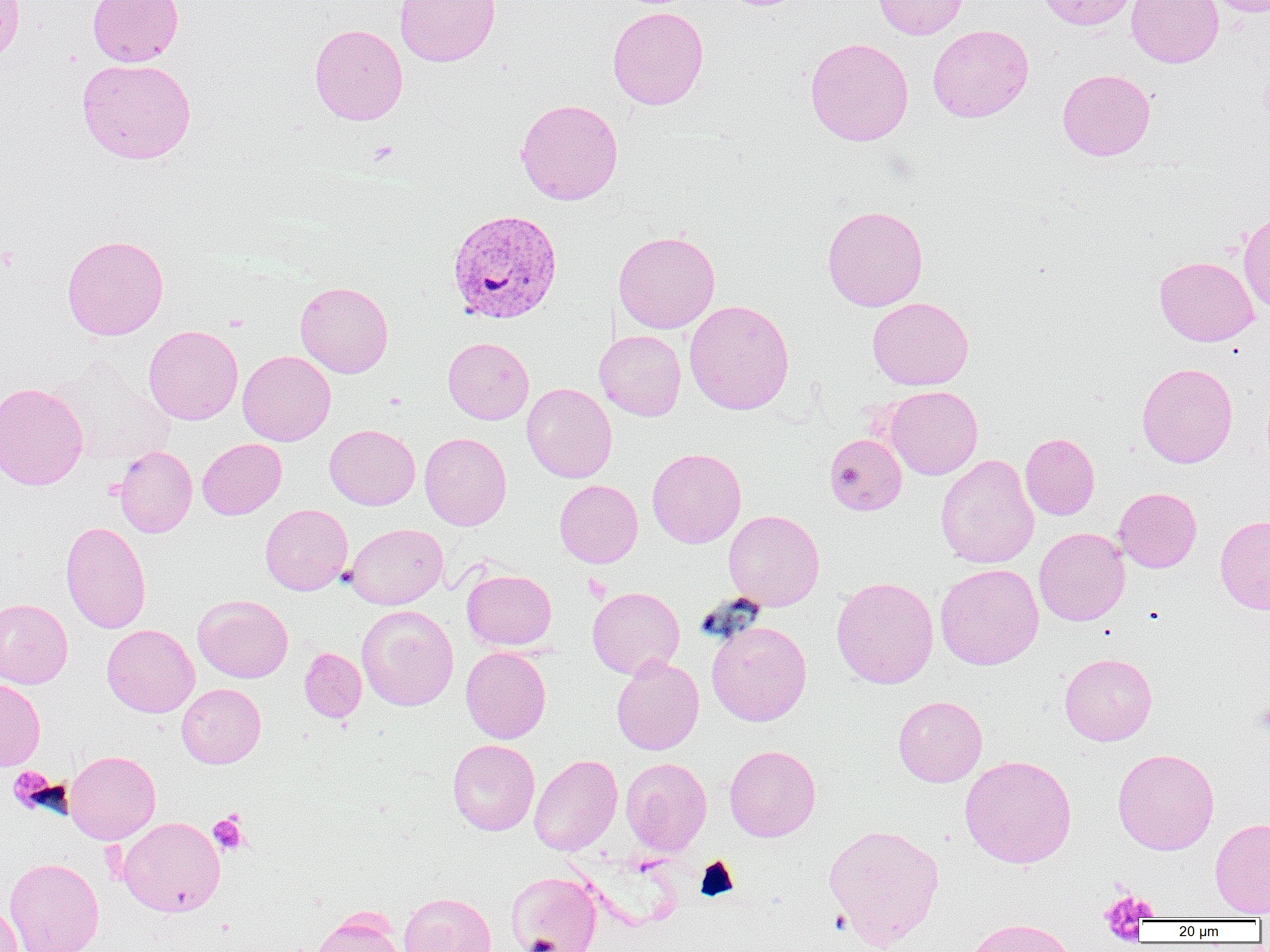

slide-level diagnosis = Plasmodium vivax
magnification = 1000x
image size = 1270×952 pixels
modality = optical microscopy
field of view = one of a larger specimen
Plasmodium vivax-infected red blood cell locations = approximate bounding boxes as (x1,y1)-(x2,y2) corner pairs in pixels: (447,209)-(563,324)
platelet locations = approximate bounding boxes as (x1,y1)-(x2,y2) corner pairs in pixels: (1258,77)-(1270,119), (368,139)-(398,165), (583,574)-(611,602), (8,767)-(63,814), (209,811)-(248,854), (1100,891)-(1155,940)
preparation = thin blood film
uninfected red blood cell locations = approximate bounding boxes as (x1,y1)-(x2,y2) corner pairs in pixels: (0,0)-(25,65), (87,0)-(183,66), (395,0)-(501,67), (873,0)-(968,39), (1037,0)-(1139,31), (1126,0)-(1224,67), (1205,0)-(1270,16), (608,6)-(709,109), (309,23)-(408,125), (927,24)-(1034,123), (805,38)-(913,146), (77,58)-(196,164), (1057,68)-(1155,161), (515,98)-(623,205), (822,204)-(928,311), (1238,211)-(1270,314), (613,230)-(720,334), (61,234)-(169,340), (1154,256)-(1259,346), (295,281)-(393,378), (867,297)-(973,390), (684,299)-(795,414), (143,325)-(243,425), (595,330)-(686,421), (443,337)-(534,424), (237,349)-(335,445), (51,361)-(174,467), (1136,362)-(1238,468), (0,381)-(88,491), (522,382)-(617,483), (885,385)-(983,480), (324,425)-(420,510), (419,432)-(511,530), (824,433)-(907,516), (1020,433)-(1100,520), (198,438)-(286,520), (113,445)-(197,537), (647,448)-(746,548), (935,453)-(1039,569), (555,479)-(643,568), (1114,487)-(1202,573), (260,503)-(353,595), (723,510)-(824,611), (1215,515)-(1270,614), (60,521)-(151,634), (345,523)-(448,610), (1034,527)-(1130,626), (935,563)-(1044,670), (462,568)-(556,650), (831,577)-(939,689), (587,586)-(684,679), (193,594)-(293,683), (0,598)-(73,688), (356,605)-(458,711), (706,620)-(811,726), (102,624)-(199,717), (461,646)-(551,744), (300,647)-(366,722), (1059,652)-(1157,745), (611,655)-(704,755), (0,677)-(46,771), (177,683)-(266,768), (893,695)-(987,787), (447,739)-(540,836), (724,744)-(821,842), (1113,748)-(1219,854), (65,750)-(160,844), (528,754)-(622,855), (960,755)-(1077,868), (621,757)-(712,856), (118,816)-(225,916), (1209,817)-(1270,917), (824,823)-(945,949), (4,857)-(103,952), (506,871)-(602,952), (399,892)-(497,952), (0,901)-(22,952), (313,913)-(405,952), (963,917)-(1080,952)